Give the extent of all uninfected red blood cells.
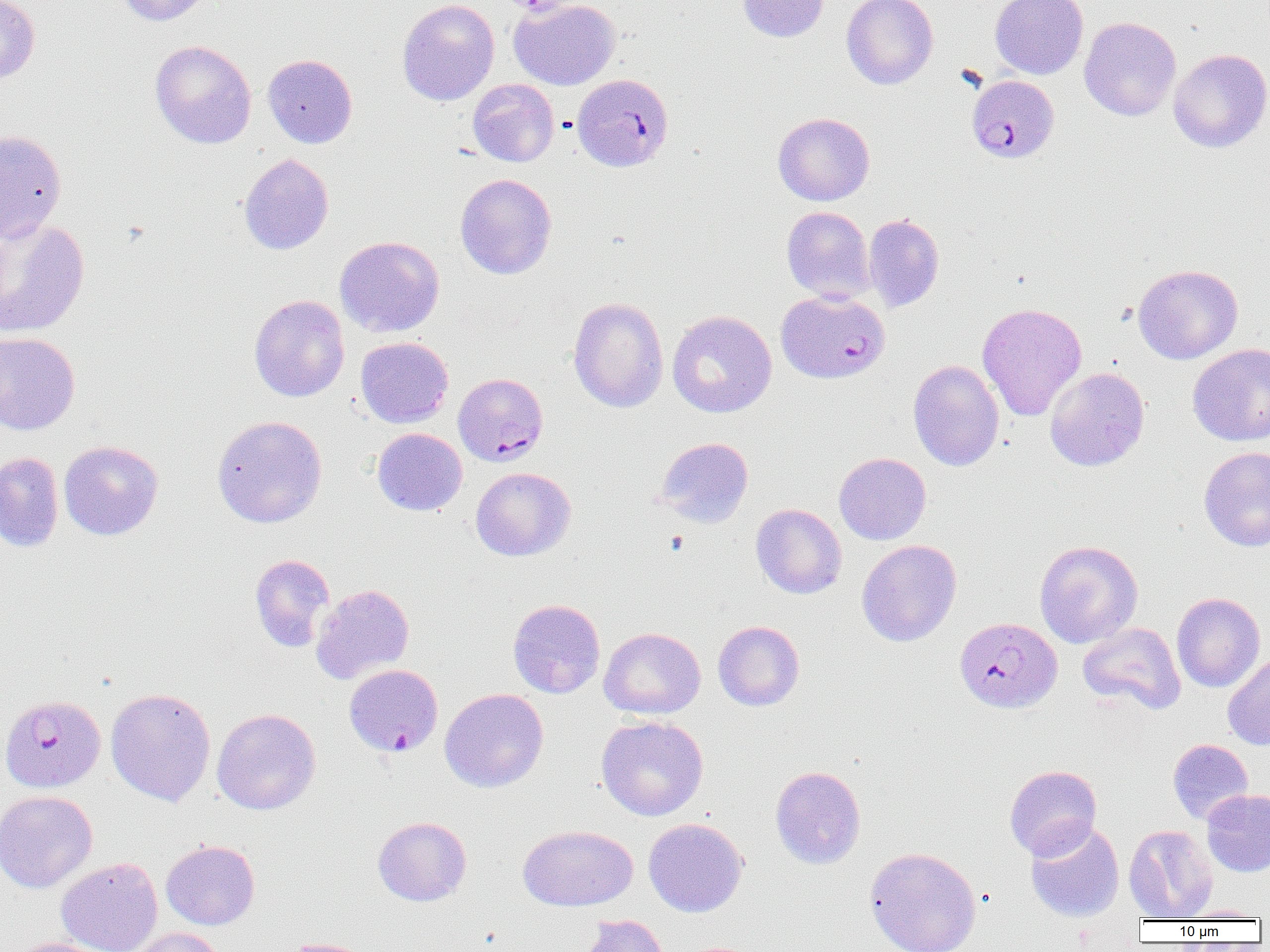

Approximate bounding boxes as (x1,y1)-(x2,y2) corner pairs in pixels.
Uninfected red blood cells: (116,0)-(217,26), (397,0)-(499,106), (509,0)-(621,90), (737,0)-(828,42), (842,0)-(938,89), (990,0)-(1088,79), (0,1)-(40,84), (1079,17)-(1181,121), (150,39)-(257,149), (1168,48)-(1270,153), (262,54)-(358,148), (467,79)-(559,167), (773,112)-(874,206), (0,130)-(67,242), (238,153)-(334,255), (455,173)-(557,279), (781,206)-(874,303), (863,214)-(945,312), (0,218)-(90,339), (335,236)-(444,337), (1133,264)-(1243,364), (249,294)-(350,402), (568,297)-(669,413), (977,303)-(1087,421), (666,310)-(777,418), (0,332)-(80,435), (355,337)-(454,428), (1188,344)-(1270,445), (908,360)-(1004,471), (1045,367)-(1150,472), (211,415)-(328,528), (372,427)-(467,516), (655,437)-(754,528), (58,440)-(163,540), (1199,446)-(1270,552), (0,452)-(63,552), (834,452)-(931,545), (471,467)-(576,561), (751,503)-(847,599), (857,539)-(962,647), (1034,540)-(1143,648), (249,554)-(335,652), (311,583)-(414,684), (1172,592)-(1265,692), (508,599)-(606,698), (713,620)-(805,711), (1078,622)-(1186,715), (599,627)-(706,719), (1222,651)-(1270,751), (105,688)-(216,806), (439,688)-(548,792), (211,708)-(321,815), (596,715)-(708,821), (1167,739)-(1253,825), (1004,765)-(1102,860), (770,766)-(866,869), (1202,789)-(1270,877), (0,790)-(98,893), (372,816)-(472,906), (643,818)-(748,917), (1025,820)-(1124,922), (518,824)-(638,911), (1123,824)-(1218,920), (161,839)-(260,930), (864,846)-(982,952), (56,857)-(163,952), (1177,906)-(1267,921), (579,915)-(668,952), (127,927)-(224,952), (281,937)-(378,952), (12,938)-(119,952).

Plasmodium falciparum-infected red blood cell locations: (572,74)-(674,172), (965,81)-(1059,166), (775,290)-(891,384), (454,373)-(548,466), (955,617)-(1061,712), (344,664)-(443,757), (1,694)-(106,792). Slide-level diagnosis: Plasmodium falciparum. Light microscopy. One field of a larger specimen. Image is 1270×952 pixels. 1000x magnification. Thin blood smear.